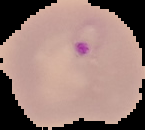
result = Plasmodium parasites identified
image size = 145×130 pixels
image type = segmented cell region with the area outside set to black
preparation = thin blood film